Report the malaria status of this cell.
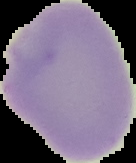

Uninfected.

Summary:
  - Image size: 136×163 pixels
  - Image type: segmented cell region with the area outside set to black
  - Preparation: thin blood film